Outline each Plasmodium parasite.
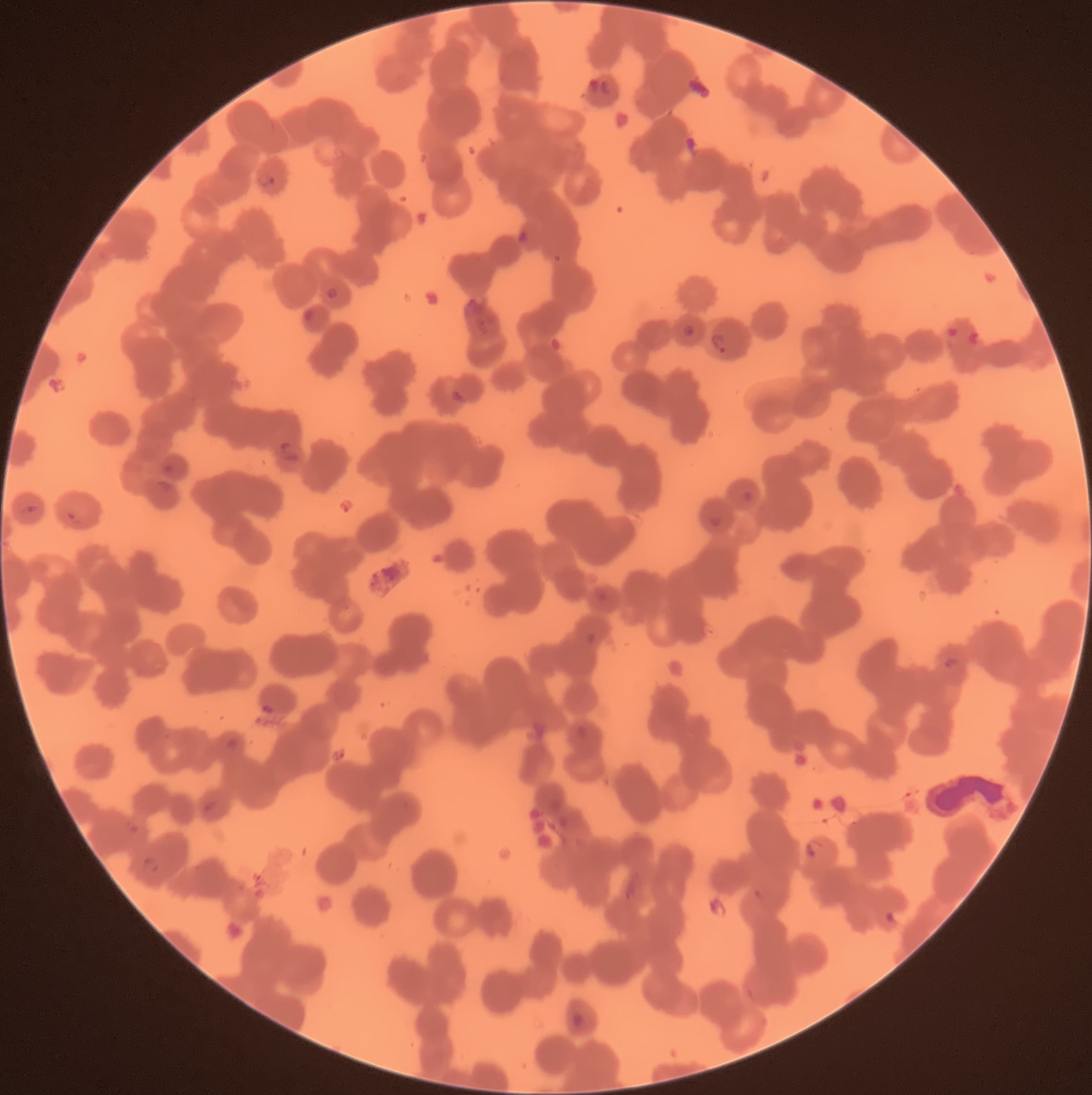

Approximate bounding boxes as named x1/y1/x2/y2 corners in pixels.
Plasmodium parasites: (x1=587, y1=78, x2=613, y2=96), (x1=258, y1=172, x2=278, y2=186), (x1=517, y1=229, x2=529, y2=244), (x1=326, y1=285, x2=340, y2=301), (x1=301, y1=308, x2=315, y2=322), (x1=682, y1=323, x2=695, y2=337), (x1=945, y1=324, x2=962, y2=339), (x1=967, y1=330, x2=979, y2=346), (x1=710, y1=332, x2=728, y2=354), (x1=449, y1=390, x2=467, y2=405), (x1=279, y1=440, x2=301, y2=463), (x1=164, y1=463, x2=176, y2=474), (x1=742, y1=490, x2=754, y2=503), (x1=21, y1=506, x2=40, y2=516), (x1=66, y1=509, x2=83, y2=526), (x1=709, y1=514, x2=722, y2=529), (x1=596, y1=588, x2=608, y2=602), (x1=944, y1=655, x2=960, y2=669), (x1=225, y1=736, x2=240, y2=751), (x1=204, y1=799, x2=219, y2=812), (x1=125, y1=818, x2=140, y2=833), (x1=804, y1=837, x2=823, y2=858), (x1=140, y1=854, x2=159, y2=876), (x1=883, y1=911, x2=896, y2=925), (x1=570, y1=1011, x2=587, y2=1027).

Summary:
  - Preparation: thin blood film
  - Image size: 1092×1095 pixels
  - Red blood cell morphology: rouleaux formation
  - Modality: optical microscopy